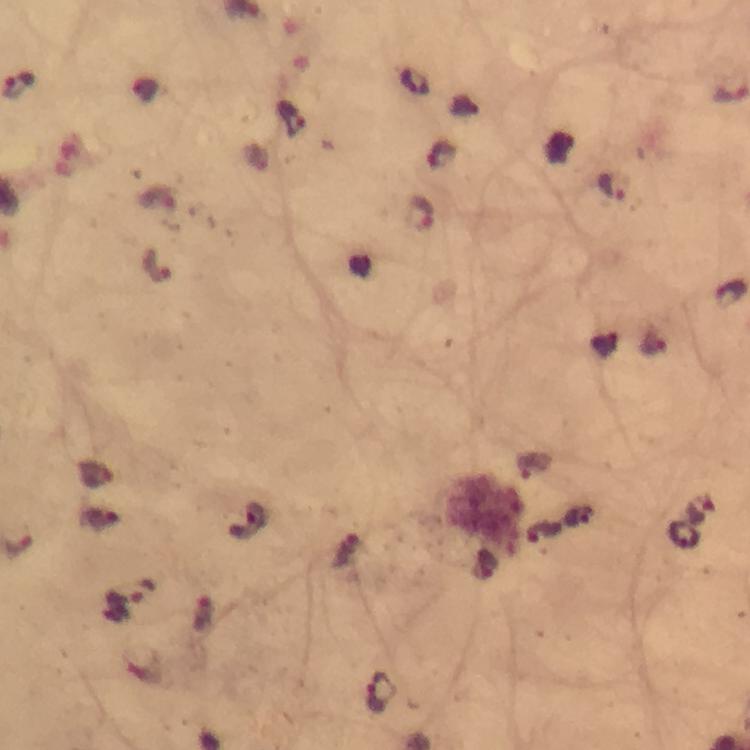
Approximate centers as [x, y] in pixels.
Summary:
  - Plasmodium parasite locations: [20, 85], [291, 118], [613, 191], [422, 214], [158, 266], [700, 511], [685, 535], [141, 593], [382, 693]
  - Immersion oil: used
  - Image size: 750×750 pixels
  - Context: from a diagnostic examination for malaria
  - Magnification: 100x
  - Preparation: thick blood smear
  - Stain: Giemsa
  - Capture: smartphone mounted on the microscope
  - Cropped from: a single field of view